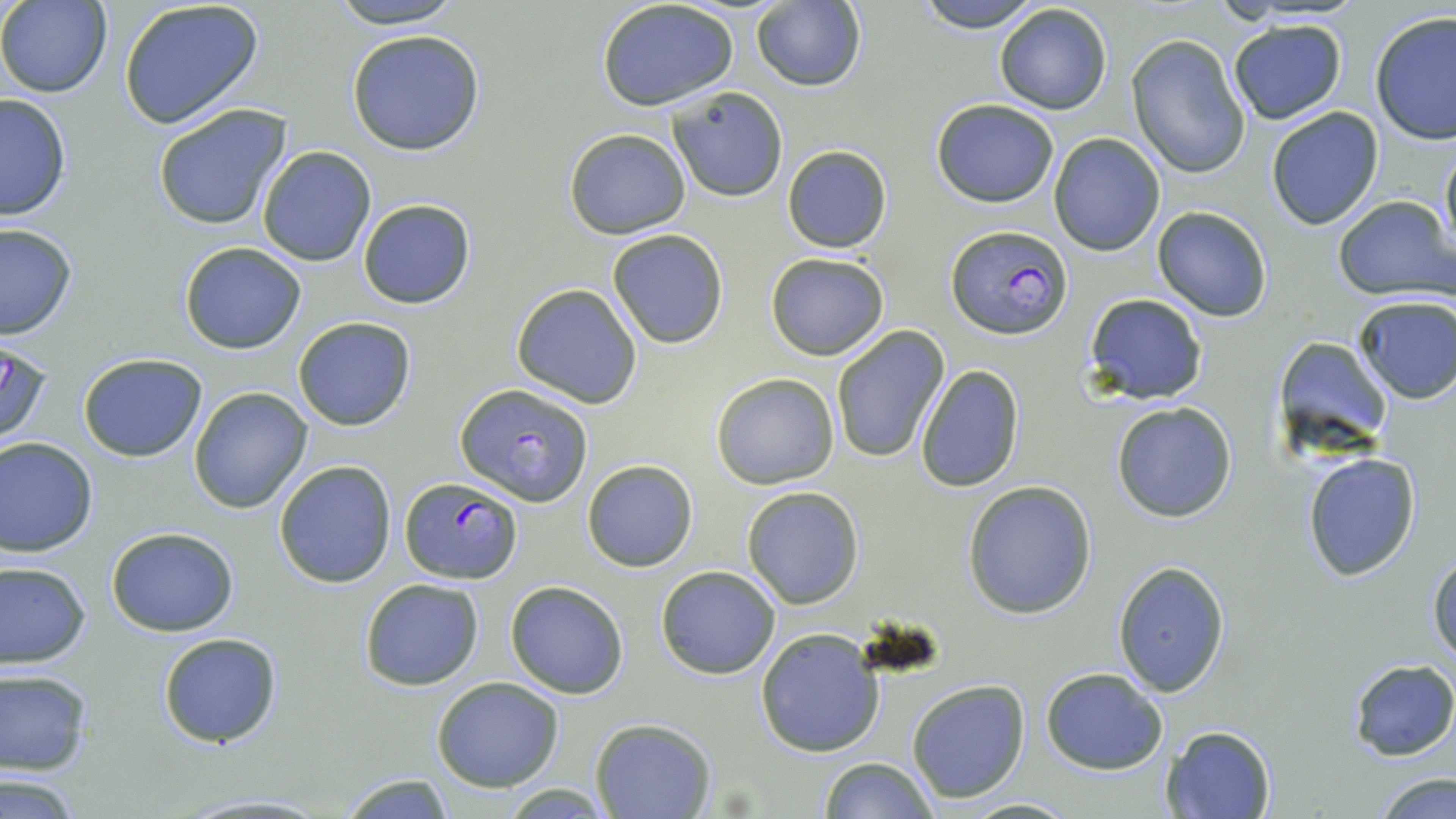

Approximate bounding boxes as [x1, y1, x2, y2] in pixels. Plasmodium falciparum-infected red blood cell locations: [947, 224, 1072, 340], [455, 382, 593, 505], [397, 478, 523, 584]. Uninfected red blood cell locations: [117, 0, 265, 129], [326, 0, 465, 28], [913, 0, 1042, 29], [0, 1, 112, 97], [598, 2, 739, 112], [750, 2, 866, 91], [993, 4, 1112, 115], [1369, 12, 1456, 144], [1228, 18, 1348, 125], [347, 28, 486, 156], [1127, 34, 1253, 180], [665, 85, 788, 202], [0, 93, 72, 223], [931, 99, 1059, 206], [152, 102, 292, 230], [1264, 106, 1384, 231], [563, 128, 691, 239], [1049, 132, 1165, 256], [1439, 138, 1456, 268], [782, 144, 894, 255], [257, 146, 377, 265], [1332, 195, 1456, 301], [358, 199, 475, 310], [1151, 206, 1274, 321], [1, 223, 77, 340], [607, 228, 729, 348], [178, 242, 306, 354], [765, 251, 890, 360], [510, 283, 643, 408], [1084, 294, 1208, 405], [1352, 294, 1456, 403], [292, 316, 417, 430], [830, 324, 950, 465], [0, 338, 54, 451], [1276, 338, 1394, 451], [77, 352, 207, 460], [916, 364, 1025, 494], [710, 372, 840, 489], [189, 386, 312, 513], [1111, 401, 1238, 521], [0, 436, 98, 557], [1302, 453, 1422, 581], [581, 459, 699, 572], [274, 460, 397, 587], [962, 479, 1097, 619], [741, 486, 864, 609], [105, 527, 239, 636], [1428, 548, 1456, 668], [0, 560, 91, 668], [1113, 561, 1231, 696], [655, 566, 781, 680], [358, 578, 485, 690], [505, 581, 629, 698], [755, 627, 885, 757], [157, 633, 282, 749], [1345, 660, 1455, 762], [1040, 667, 1168, 773], [0, 669, 93, 775], [431, 677, 563, 790], [906, 678, 1030, 803], [589, 717, 715, 819], [1160, 725, 1276, 818], [817, 757, 937, 819], [335, 772, 458, 817], [1374, 772, 1455, 819], [0, 774, 86, 816], [956, 796, 1079, 817]. Slide-level diagnosis: Plasmodium falciparum. Light microscopy. One field of a larger specimen. Thin blood smear. Image is 1456×819 pixels. Captured at 1000x magnification. May-Grünwald-Giemsa-stained preparation.